Assess this cell for malaria.
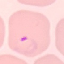
It is parasitized.

Summary:
  - Image type: automatically extracted cell patch, resized to 64 × 64 pixels
  - Preparation: thin blood smear
  - Stain: Giemsa
  - Capture: smartphone camera at the microscope eyepiece